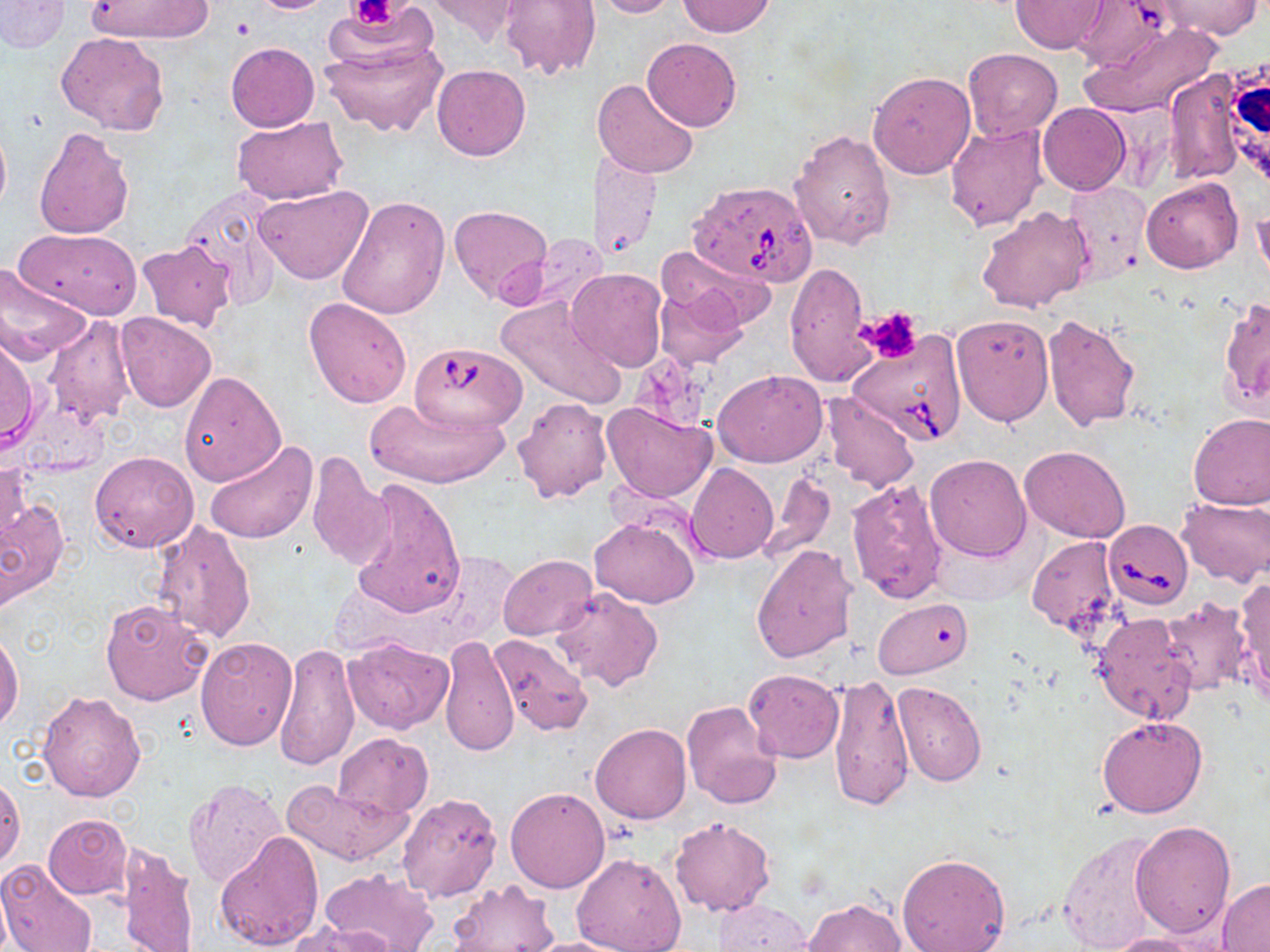
Summary:
  - Coordinate format: approximate bounding boxes as named x1/y1/x2/y2 corners in pixels
  - Uninfected red blood cell locations: (x1=0, y1=0, x2=70, y2=53), (x1=84, y1=0, x2=213, y2=42), (x1=248, y1=0, x2=338, y2=14), (x1=328, y1=0, x2=440, y2=74), (x1=500, y1=0, x2=599, y2=79), (x1=587, y1=0, x2=678, y2=18), (x1=1154, y1=0, x2=1261, y2=40), (x1=421, y1=1, x2=532, y2=45), (x1=678, y1=1, x2=775, y2=37), (x1=1011, y1=1, x2=1107, y2=53), (x1=1069, y1=1, x2=1175, y2=74), (x1=1084, y1=21, x2=1222, y2=121), (x1=318, y1=30, x2=448, y2=137), (x1=55, y1=32, x2=169, y2=138), (x1=642, y1=38, x2=742, y2=131), (x1=226, y1=42, x2=319, y2=132), (x1=963, y1=48, x2=1062, y2=140), (x1=432, y1=64, x2=530, y2=160), (x1=1162, y1=69, x2=1249, y2=187), (x1=867, y1=71, x2=976, y2=179), (x1=592, y1=78, x2=699, y2=180), (x1=1037, y1=103, x2=1130, y2=195), (x1=233, y1=116, x2=348, y2=205), (x1=0, y1=118, x2=11, y2=224), (x1=945, y1=123, x2=1050, y2=231), (x1=34, y1=127, x2=135, y2=241), (x1=789, y1=129, x2=896, y2=250), (x1=590, y1=152, x2=662, y2=259), (x1=1141, y1=178, x2=1243, y2=273), (x1=1063, y1=180, x2=1154, y2=284), (x1=253, y1=184, x2=373, y2=285), (x1=180, y1=189, x2=284, y2=308), (x1=335, y1=194, x2=450, y2=321), (x1=1251, y1=202, x2=1269, y2=286), (x1=977, y1=205, x2=1096, y2=314), (x1=449, y1=206, x2=552, y2=303), (x1=13, y1=229, x2=141, y2=320), (x1=516, y1=232, x2=612, y2=314), (x1=136, y1=239, x2=237, y2=332), (x1=658, y1=240, x2=777, y2=330), (x1=784, y1=260, x2=874, y2=388), (x1=0, y1=266, x2=92, y2=366), (x1=567, y1=268, x2=667, y2=370), (x1=654, y1=285, x2=747, y2=371), (x1=496, y1=295, x2=627, y2=410), (x1=303, y1=296, x2=413, y2=409), (x1=1218, y1=297, x2=1270, y2=416), (x1=116, y1=312, x2=216, y2=412), (x1=951, y1=314, x2=1055, y2=427), (x1=1042, y1=315, x2=1141, y2=431), (x1=43, y1=317, x2=136, y2=428), (x1=0, y1=336, x2=40, y2=451), (x1=713, y1=368, x2=827, y2=467), (x1=178, y1=372, x2=284, y2=485), (x1=821, y1=393, x2=920, y2=493), (x1=366, y1=395, x2=510, y2=488), (x1=512, y1=397, x2=612, y2=502), (x1=601, y1=401, x2=717, y2=503), (x1=1187, y1=412, x2=1270, y2=512), (x1=204, y1=440, x2=318, y2=544), (x1=1019, y1=445, x2=1131, y2=543), (x1=90, y1=451, x2=198, y2=553), (x1=305, y1=453, x2=393, y2=570), (x1=925, y1=454, x2=1031, y2=562), (x1=0, y1=460, x2=31, y2=546), (x1=686, y1=463, x2=778, y2=562), (x1=762, y1=471, x2=836, y2=564), (x1=347, y1=477, x2=465, y2=618), (x1=846, y1=478, x2=950, y2=604), (x1=0, y1=497, x2=69, y2=608), (x1=1177, y1=497, x2=1270, y2=584), (x1=590, y1=517, x2=699, y2=608), (x1=150, y1=521, x2=257, y2=644), (x1=1026, y1=535, x2=1121, y2=634), (x1=751, y1=544, x2=856, y2=664), (x1=498, y1=554, x2=597, y2=641), (x1=1233, y1=578, x2=1270, y2=704), (x1=550, y1=586, x2=665, y2=692), (x1=872, y1=598, x2=973, y2=679), (x1=1158, y1=599, x2=1251, y2=694), (x1=100, y1=600, x2=212, y2=705), (x1=1089, y1=612, x2=1195, y2=722), (x1=1, y1=631, x2=22, y2=732), (x1=439, y1=635, x2=519, y2=757), (x1=487, y1=635, x2=594, y2=736), (x1=194, y1=636, x2=296, y2=750), (x1=344, y1=637, x2=453, y2=733), (x1=272, y1=642, x2=360, y2=772), (x1=744, y1=669, x2=844, y2=762), (x1=828, y1=674, x2=915, y2=811), (x1=892, y1=682, x2=986, y2=786), (x1=36, y1=690, x2=146, y2=802), (x1=681, y1=699, x2=785, y2=810), (x1=1097, y1=715, x2=1207, y2=819), (x1=590, y1=723, x2=691, y2=823), (x1=334, y1=732, x2=433, y2=819), (x1=0, y1=772, x2=25, y2=870), (x1=183, y1=776, x2=289, y2=891), (x1=282, y1=778, x2=412, y2=867), (x1=505, y1=786, x2=611, y2=893), (x1=396, y1=792, x2=504, y2=905), (x1=42, y1=814, x2=132, y2=899), (x1=670, y1=817, x2=777, y2=917), (x1=1130, y1=821, x2=1236, y2=940), (x1=1058, y1=831, x2=1166, y2=952), (x1=214, y1=832, x2=324, y2=951), (x1=117, y1=841, x2=198, y2=952), (x1=571, y1=851, x2=686, y2=952), (x1=896, y1=852, x2=1010, y2=952), (x1=0, y1=859, x2=98, y2=952), (x1=318, y1=866, x2=437, y2=952), (x1=447, y1=879, x2=560, y2=951), (x1=1217, y1=880, x2=1270, y2=950), (x1=803, y1=897, x2=904, y2=952), (x1=713, y1=898, x2=814, y2=951), (x1=292, y1=922, x2=394, y2=951), (x1=1104, y1=931, x2=1224, y2=952), (x1=518, y1=936, x2=642, y2=952)
  - Babesia divergens-infected red blood cell locations: (x1=687, y1=179, x2=819, y2=289), (x1=849, y1=330, x2=969, y2=445), (x1=411, y1=342, x2=529, y2=436), (x1=1104, y1=518, x2=1191, y2=610)
  - Platelet locations: (x1=351, y1=0, x2=398, y2=27), (x1=861, y1=307, x2=923, y2=363)
  - Slide-level diagnosis: Babesia divergens
  - Image size: 1270×952 pixels
  - Preparation: thin blood film
  - Modality: light microscopy
  - Field of view: single
  - Stain: May-Grünwald-Giemsa
  - Magnification: 1000x